State which parasite is depicted.
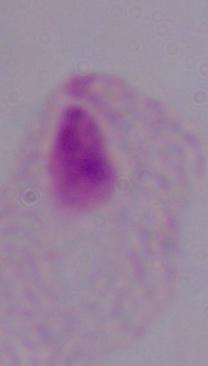

This is a trichomonad.

magnification = 1000x
modality = photomicrograph